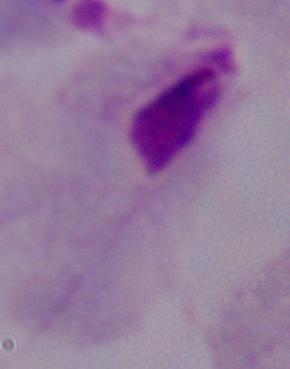

Summary:
  - Identification: trichomonad
  - Modality: photomicrograph
  - Magnification: 1000x